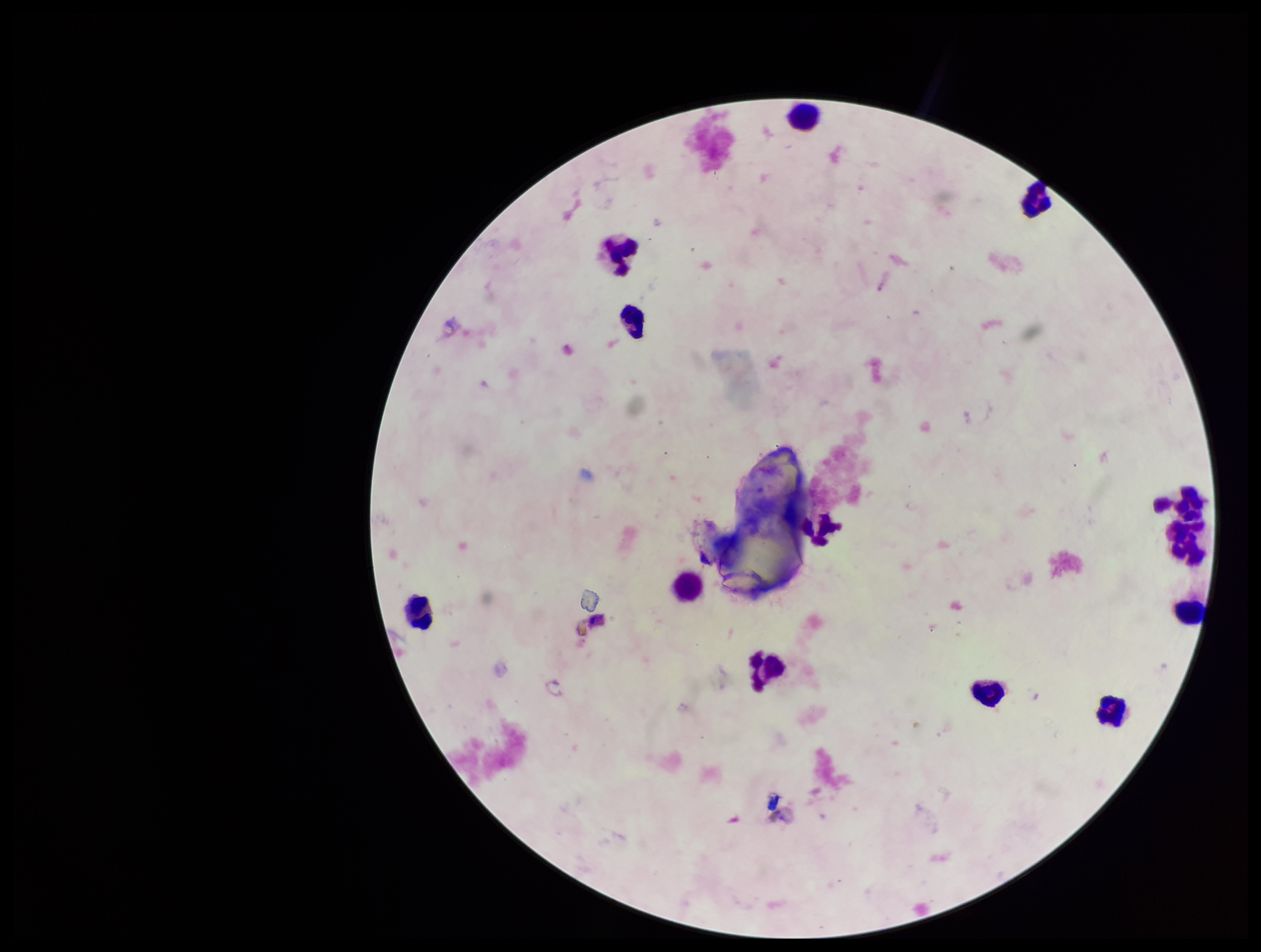

Image is 1261×952 pixels. Leukocyte count: 13. Patient malaria status: negative. Parasite count: 0. Giemsa stain. Smartphone photograph taken through the eyepiece of a microscope. Plasmodium parasites: none detected. Single field of view. Preparation: thick blood smear.